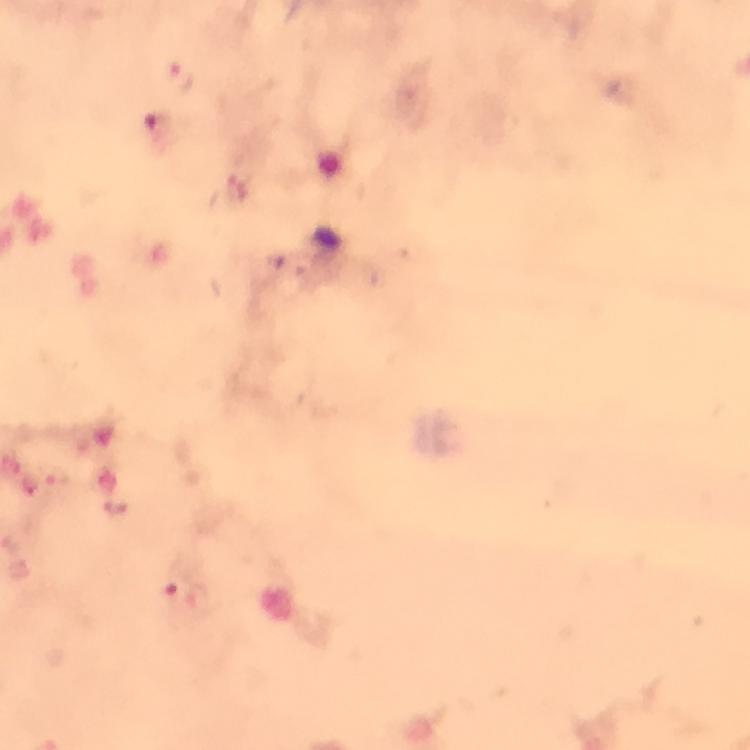

Approximate object centers, in pixels from the top-left corner.
Summary:
  - Plasmodium parasite locations: (x=179, y=76), (x=200, y=597)
  - Capture: smartphone mounted on the microscope
  - Image size: 750×750 pixels
  - Context: from a malaria diagnostic workup
  - Stain: Giemsa
  - Cropped from: a single field of view
  - Preparation: thick blood film
  - Immersion oil: applied
  - Magnification: 100x